Report the malaria status of this cell.
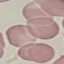
It is uninfected.

Summary:
  - Stain: Giemsa
  - Capture: smartphone through the microscope eyepiece
  - Image type: automatically extracted cell patch, resized to 64 × 64 pixels
  - Preparation: thin blood smear